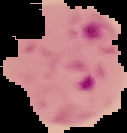

{
  "image_type": "segmented cell region with the area outside set to black",
  "preparation": "thin blood smear",
  "image_size": "127×133 pixels",
  "malaria_status": "parasitized"
}